Classify this cell by malaria status.
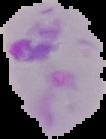
Parasitized.

image size = 106×139 pixels
preparation = thin blood smear
image type = segmented cell region on a black background